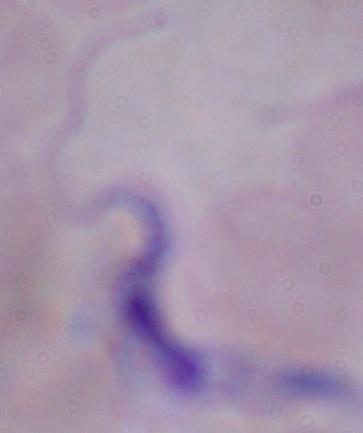 Captured at 1000x magnification. Micrograph. A trypanosome is seen.